Comment on the morphology of the erythrocytes.
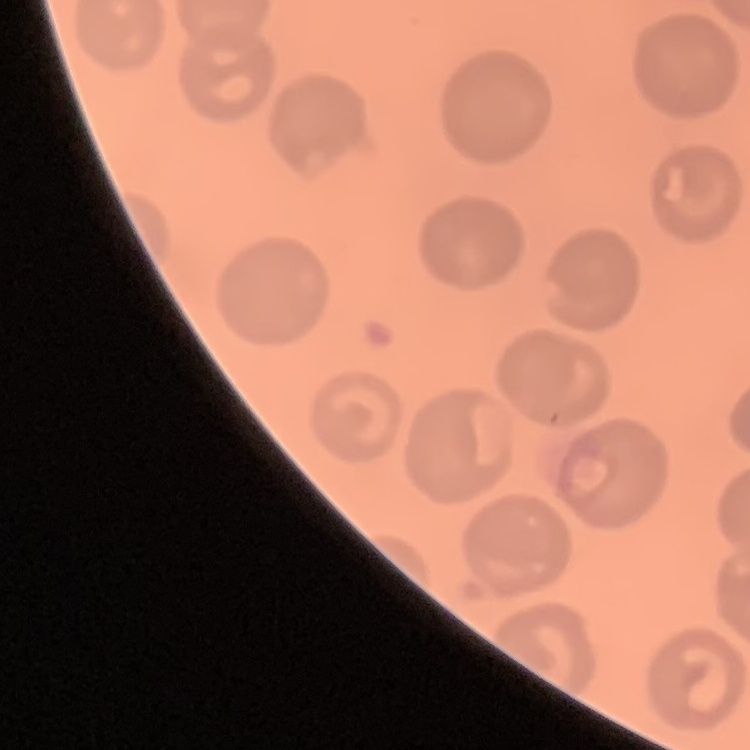
No rouleaux formation.

Field's or Giemsa stain. One tile cut from a larger photomicrograph. Thin blood smear.